Report the malaria status of this cell.
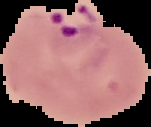

Parasitized.

Summary:
  - Image size: 151×127 pixels
  - Preparation: thin blood smear
  - Image type: cell region segmented out of the field of view; surrounding area masked to black